Look for Plasmodium parasites.
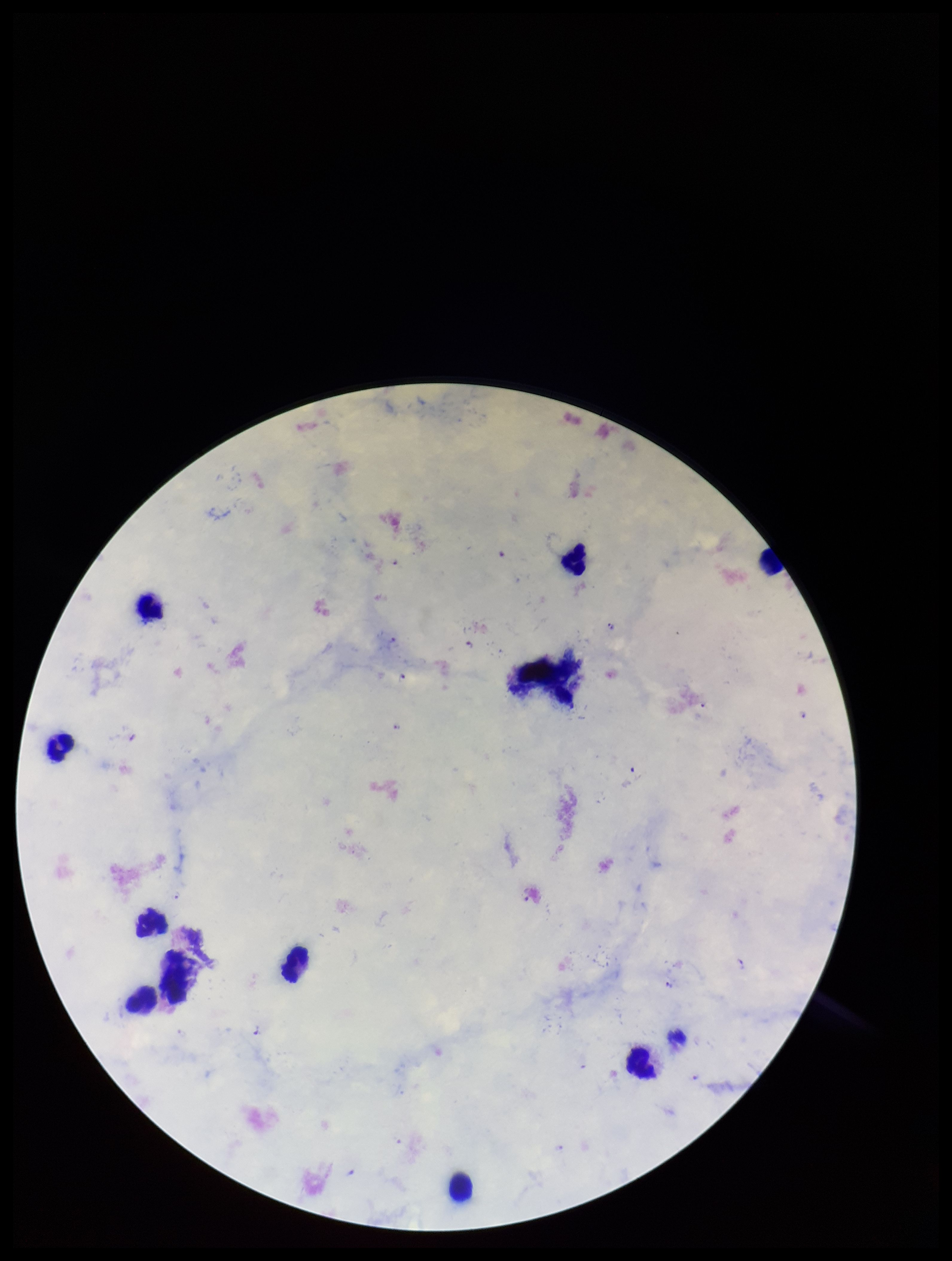

Detected.

leukocyte count = 11
capture = smartphone photograph through the microscope eyepiece
field of view = single
stain = Giemsa
patient malaria status = positive
species reported for this patient = Plasmodium falciparum
image size = 952×1261 pixels
parasite count = 5
preparation = thick smear